Comment on the morphology of the erythrocytes.
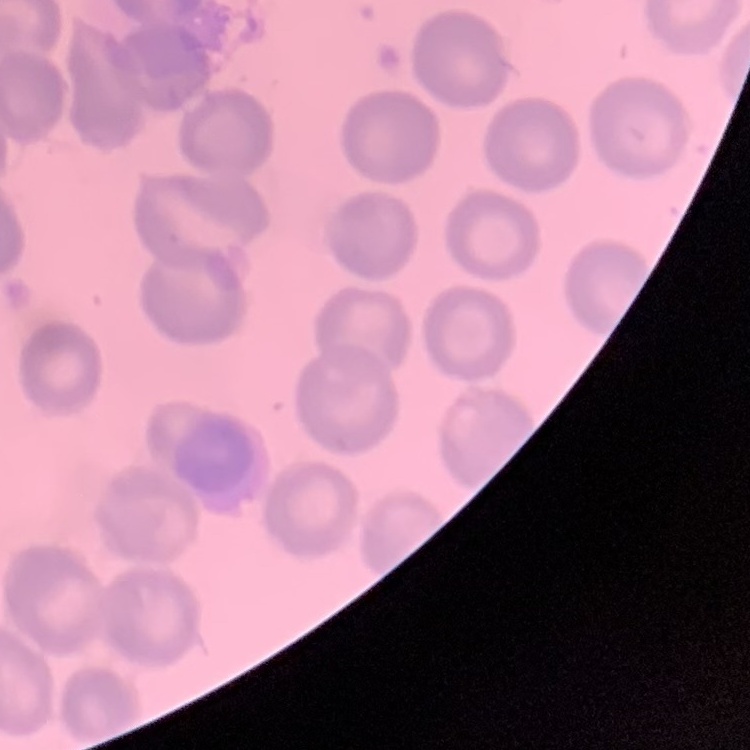
They show no rouleaux formation.

Summary:
  - Preparation: thin blood smear
  - Image type: square crop of a larger photomicrograph
  - Stain: Field's or Giemsa